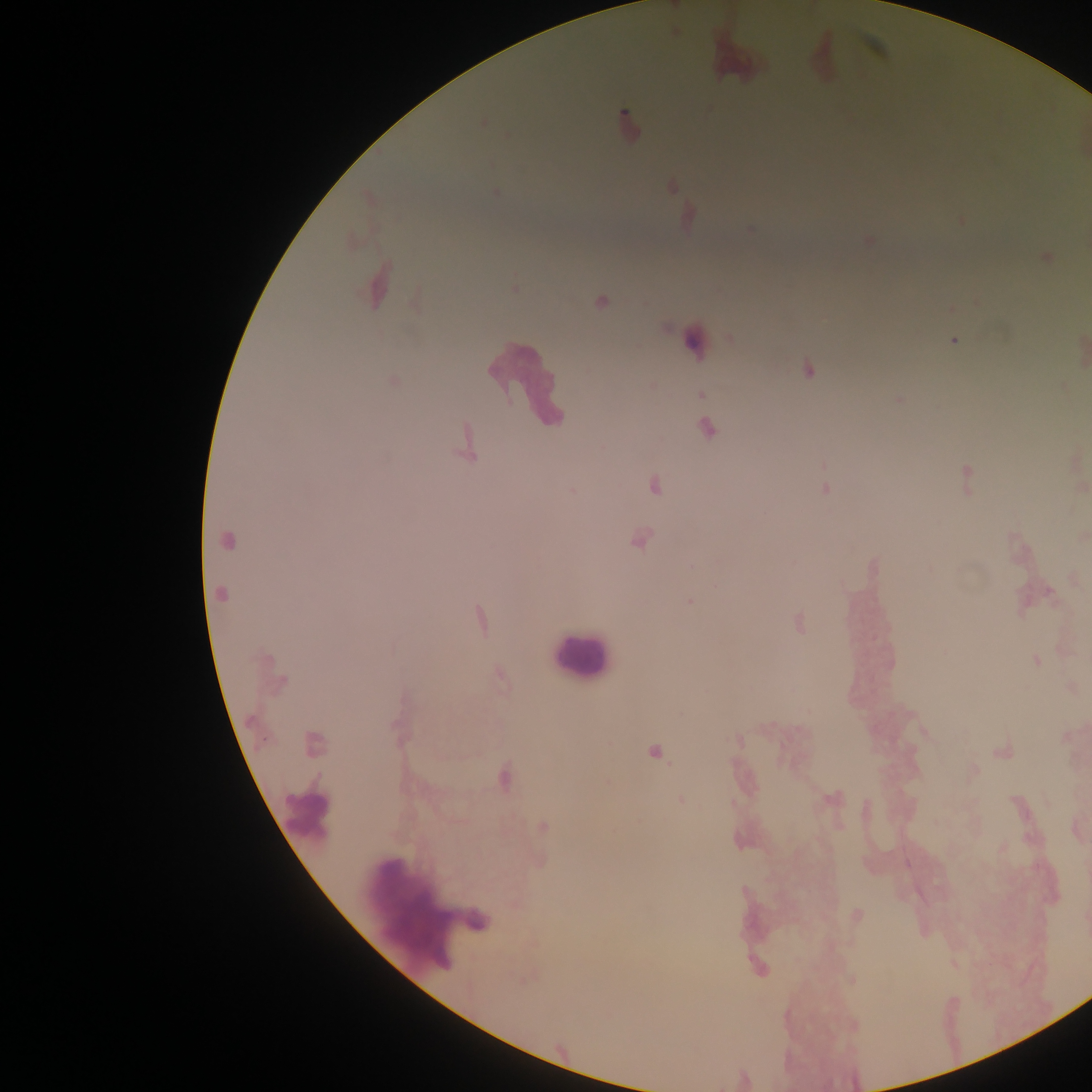

field of view = single
Plasmodium parasite locations = approximate centers as [x, y] in pixels: [628, 121], [484, 124], [495, 192], [1046, 258], [376, 287], [514, 288], [601, 302], [954, 341], [808, 370], [701, 395], [899, 400], [707, 428], [468, 445], [967, 478], [654, 486], [826, 489], [639, 540], [227, 541], [692, 567], [1050, 593], [221, 594], [690, 601], [480, 619], [800, 624], [1036, 661], [282, 681], [739, 741], [314, 744], [654, 752], [1003, 752], [504, 777], [681, 799], [831, 799], [543, 827], [1003, 848]
image size = 1092×1092 pixels
object labeled both Plasmodium parasite and leukocyte by the source = approximate centers as [x, y] in pixels: [693, 342]
leukocyte locations = approximate centers as [x, y] in pixels: [737, 54], [821, 56], [529, 382], [579, 657], [307, 815], [425, 905]
capture = mobile-phone photograph through a microscope
country = Ghana
preparation = thick blood smear